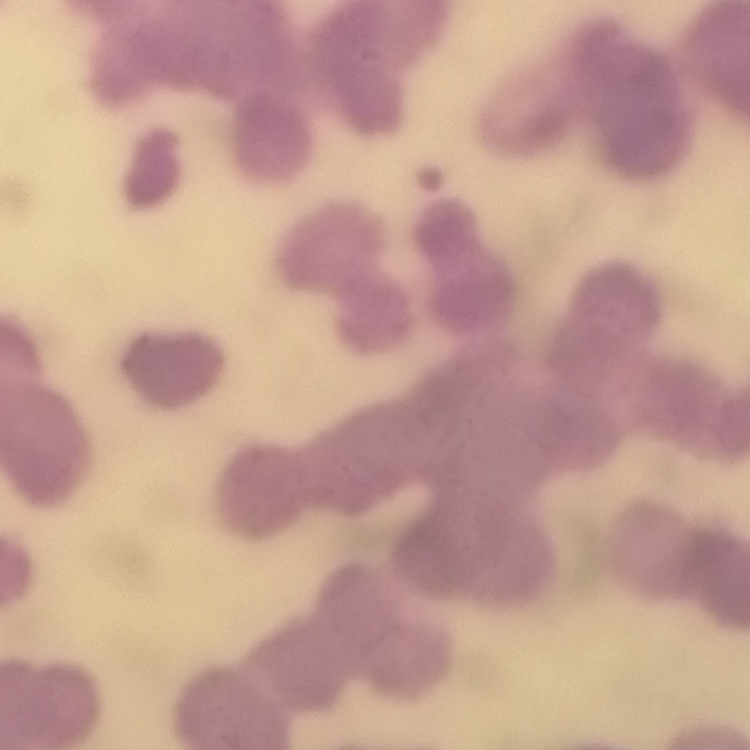
Summary:
  - Erythrocyte morphology: rouleaux formation
  - Stain: Field's or Giemsa
  - Image type: square crop of a larger photomicrograph
  - Preparation: thin peripheral smear